Report the malaria status of this cell.
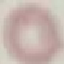
It is uninfected.

stain = Giemsa
image type = automatically extracted cell patch, resized to 64 × 64 pixels
preparation = thin blood smear
capture = smartphone camera at the microscope eyepiece